Name the cell type shown.
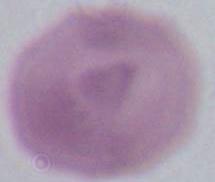

An erythrocyte.

Micrograph. Captured at 1000x magnification.